Locate and identify every blood parasite.
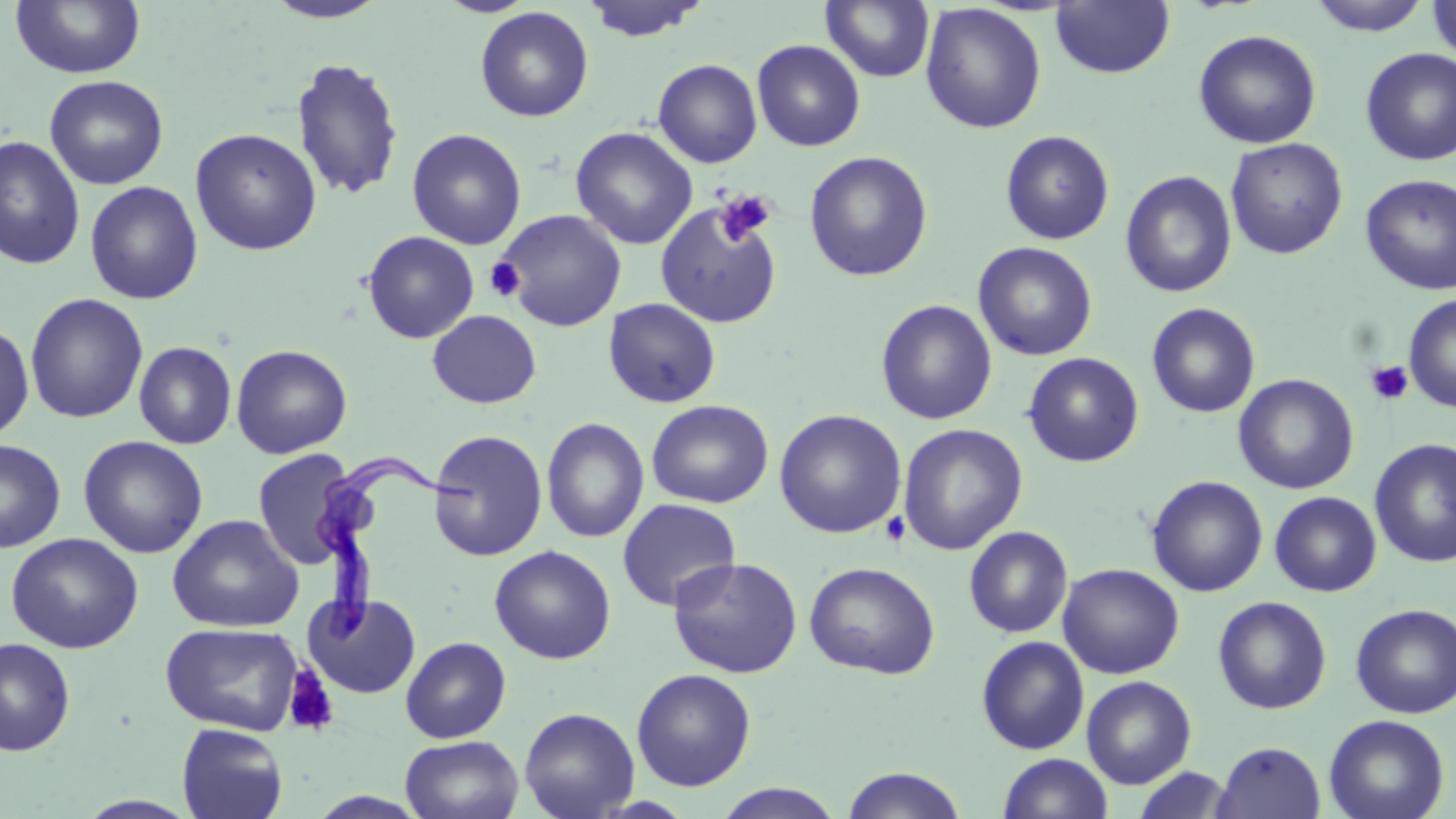
Approximate bounding boxes as [x1, y1, x2, y2] in pixels.
Trypanosoma brucei: [314, 452, 479, 655].
No Plasmodium falciparum, Plasmodium ovale, Plasmodium malariae, Plasmodium vivax, or Babesia divergens observed.

slide-level diagnosis = Trypanosoma brucei
magnification = 1000x
uninfected red blood cell locations = approximate bounding boxes as [x1, y1, x2, y2] in pixels: [10, 0, 146, 79], [437, 0, 537, 17], [580, 0, 709, 42], [821, 0, 935, 83], [1306, 0, 1433, 36], [1426, 0, 1456, 65], [262, 1, 392, 24], [1051, 1, 1175, 79], [920, 3, 1046, 133], [475, 6, 593, 122], [1193, 29, 1322, 149], [752, 39, 866, 152], [1360, 47, 1456, 165], [291, 56, 404, 202], [653, 59, 763, 168], [44, 75, 168, 190], [189, 127, 322, 256], [571, 127, 698, 249], [407, 128, 526, 249], [1000, 129, 1115, 245], [0, 136, 84, 270], [1225, 137, 1348, 260], [804, 151, 933, 281], [1120, 170, 1237, 298], [1360, 173, 1456, 295], [84, 180, 203, 305], [654, 200, 782, 328], [495, 209, 627, 332], [361, 231, 480, 344], [973, 242, 1098, 361], [25, 292, 148, 424], [1403, 294, 1456, 413], [603, 298, 721, 408], [876, 300, 997, 425], [1147, 302, 1261, 418], [427, 310, 541, 409], [0, 321, 35, 442], [134, 341, 237, 450], [231, 344, 352, 459], [1023, 352, 1144, 467], [1233, 374, 1359, 494], [646, 399, 773, 508], [774, 409, 907, 539], [542, 417, 649, 543], [897, 423, 1028, 555], [428, 429, 548, 561], [78, 435, 209, 559], [1369, 437, 1456, 568], [0, 439, 66, 553], [252, 449, 357, 570], [1146, 475, 1268, 597], [1269, 491, 1381, 597], [617, 498, 741, 611], [167, 514, 304, 633], [963, 525, 1073, 638], [5, 532, 144, 654], [489, 545, 616, 664], [667, 556, 803, 678], [804, 561, 940, 679], [1058, 563, 1184, 679], [303, 592, 421, 699], [1212, 596, 1332, 714], [1350, 603, 1455, 719], [160, 622, 303, 736], [400, 636, 511, 743], [976, 636, 1090, 754], [1, 637, 75, 756], [631, 668, 756, 791], [1081, 675, 1197, 789], [519, 707, 639, 819], [1324, 714, 1449, 819], [176, 723, 288, 819], [400, 734, 524, 819], [1213, 741, 1326, 819], [998, 753, 1113, 818], [840, 766, 968, 819], [1131, 766, 1235, 818], [712, 783, 846, 818]
modality = light microscopy
field of view = one of a larger specimen
stain = May-Grünwald-Giemsa
platelet locations = approximate bounding boxes as [x1, y1, x2, y2] in pixels: [687, 187, 781, 274], [714, 190, 776, 247], [485, 257, 525, 301], [1365, 360, 1414, 406], [881, 511, 911, 547], [283, 666, 338, 736]
image size = 1456×819 pixels
preparation = thin blood smear